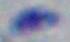
Photomicrograph. 1000x magnification. Toxoplasma gondii is shown.